Locate every Plasmodium ovale-infected red blood cell.
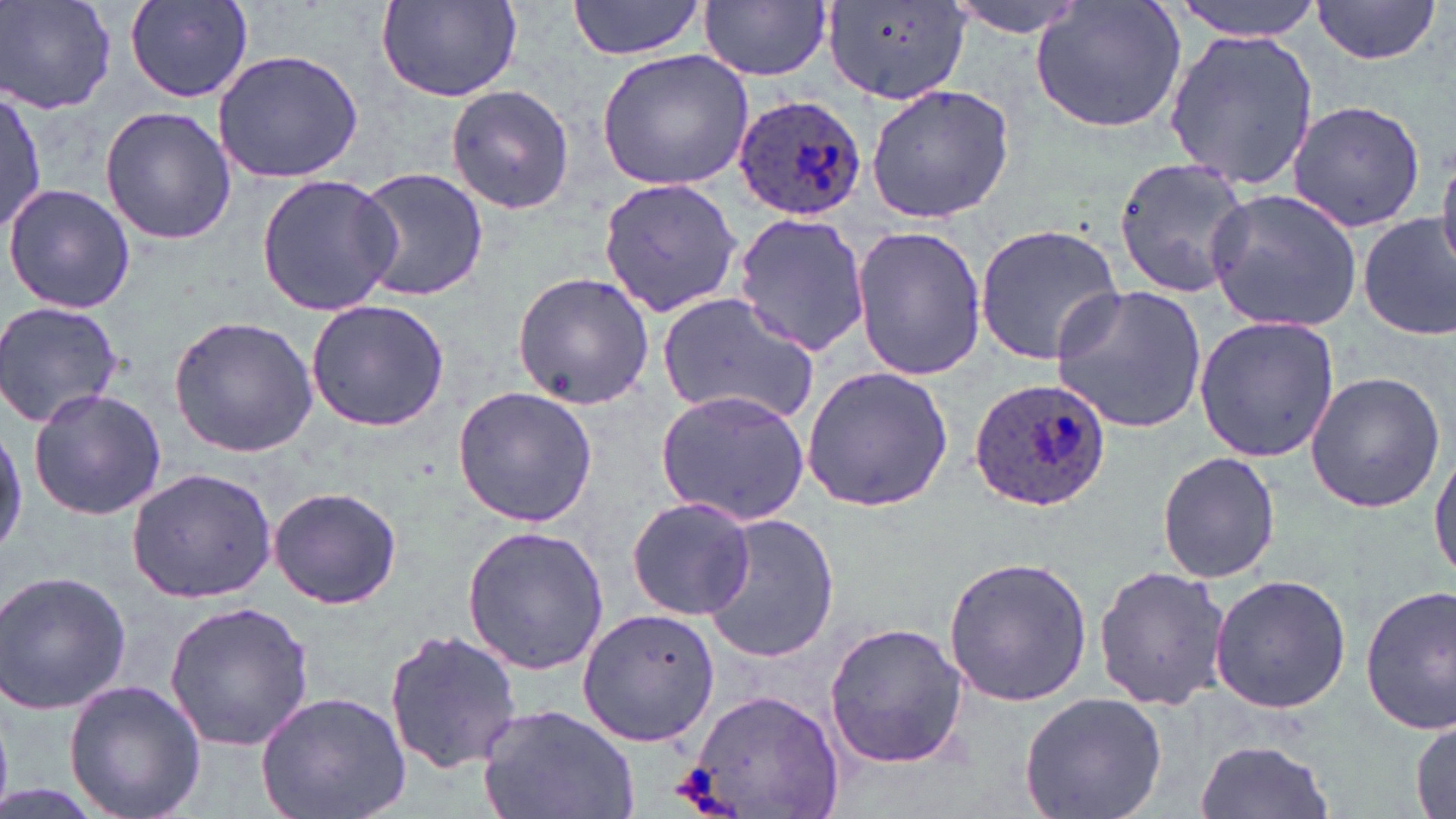

Approximate bounding boxes as [x1, y1, x2, y2] in pixels.
Plasmodium ovale-infected red blood cells: [731, 93, 868, 220], [967, 376, 1112, 511].

{
  "slide_level_diagnosis": "Plasmodium ovale",
  "preparation": "thin blood film",
  "magnification": "1000x",
  "image_size": "1456×819 pixels",
  "modality": "optical microscopy",
  "stain": "May-Grünwald-Giemsa",
  "field_of_view": "one of a larger specimen",
  "uninfected_red_blood_cell_locations": "approximate bounding boxes as [x1, y1, x2, y2] in pixels: [123, 0, 258, 104], [569, 0, 708, 59], [941, 0, 1100, 38], [1167, 0, 1324, 39], [1311, 0, 1442, 67], [0, 1, 119, 112], [700, 1, 830, 81], [375, 2, 522, 101], [1029, 2, 1187, 135], [824, 3, 972, 105], [1163, 27, 1320, 190], [210, 49, 364, 183], [595, 49, 754, 191], [445, 84, 575, 215], [865, 84, 1016, 223], [0, 89, 45, 238], [1285, 99, 1427, 232], [100, 106, 236, 246], [1437, 150, 1456, 277], [1111, 155, 1252, 299], [353, 166, 488, 302], [255, 171, 401, 317], [597, 176, 742, 320], [4, 183, 135, 315], [1204, 188, 1364, 330], [732, 211, 872, 357], [1357, 213, 1454, 339], [972, 223, 1126, 365], [850, 224, 988, 382], [512, 272, 656, 411], [1050, 284, 1210, 434], [656, 293, 821, 427], [1, 300, 125, 428], [305, 300, 449, 431], [167, 313, 319, 457], [1193, 314, 1341, 462], [800, 366, 955, 514], [1304, 369, 1448, 515], [451, 386, 598, 527], [27, 387, 167, 521], [655, 389, 811, 526], [0, 422, 25, 559], [1430, 438, 1456, 589], [1156, 452, 1281, 586], [127, 468, 277, 600], [269, 485, 404, 609], [629, 495, 756, 621], [696, 515, 841, 664], [461, 525, 611, 676], [942, 556, 1093, 709], [1093, 564, 1230, 712], [0, 568, 132, 716], [1208, 574, 1352, 714], [1359, 586, 1456, 733], [163, 600, 315, 751], [576, 608, 719, 746], [823, 620, 969, 770], [382, 627, 521, 773], [63, 677, 207, 819], [684, 685, 844, 818], [255, 689, 412, 819], [1018, 691, 1169, 819], [477, 701, 639, 819], [1412, 715, 1454, 817], [1194, 738, 1334, 819], [0, 784, 111, 819]"
}